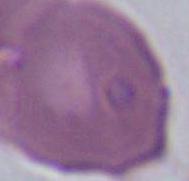

Summary:
  - Identification: erythrocyte
  - Modality: micrograph
  - Magnification: 1000x